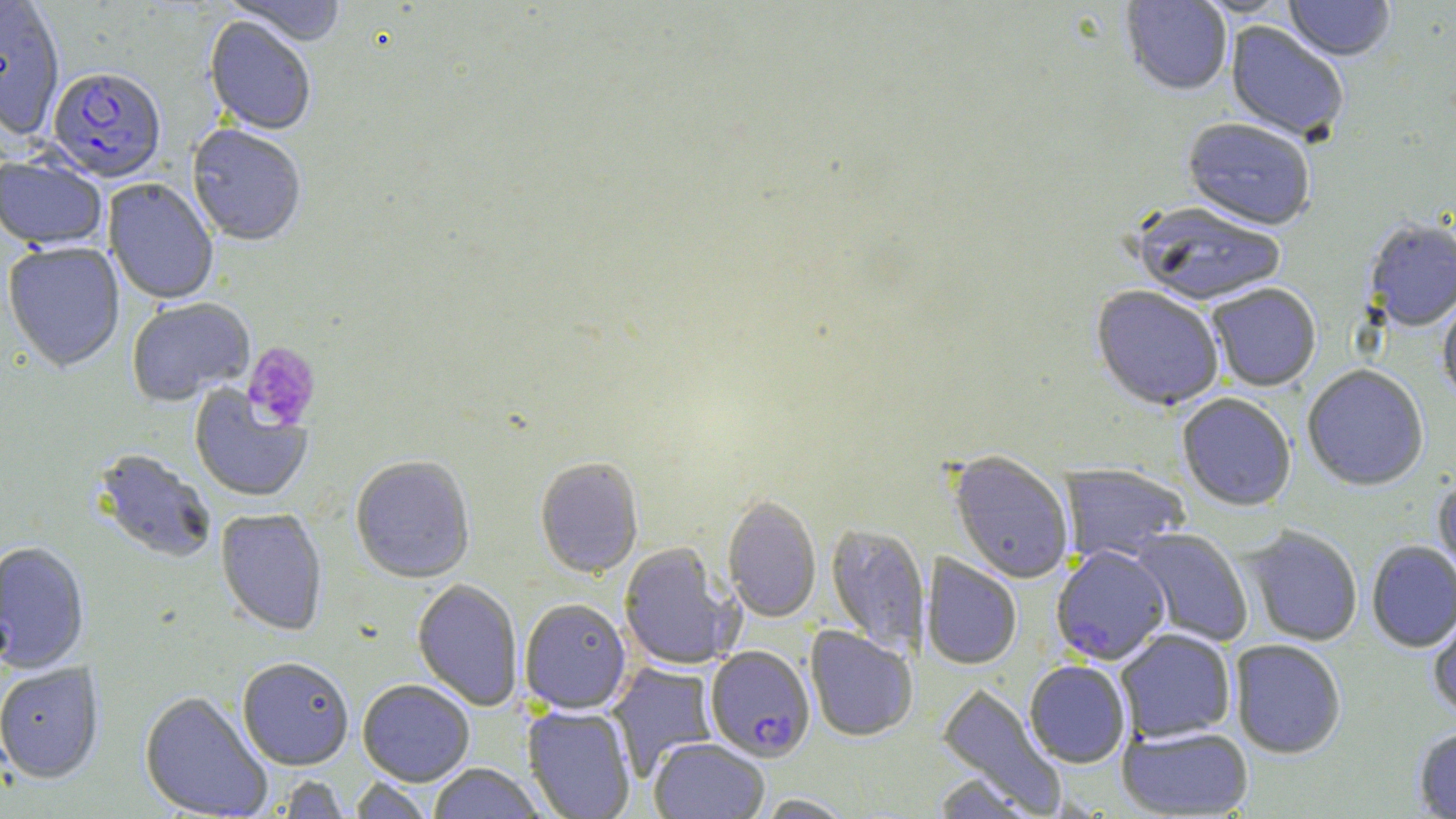
slide-level diagnosis = Plasmodium falciparum
platelet locations = approximate bounding boxes as [x1, y1, x2, y2] in pixels: [242, 341, 321, 431]
Plasmodium falciparum-infected red blood cell locations = approximate bounding boxes as [x1, y1, x2, y2] in pixels: [47, 69, 166, 186], [1051, 546, 1170, 664], [705, 646, 815, 762]
stain = May-Grünwald-Giemsa
preparation = thin blood film
modality = optical microscopy
uninfected red blood cell locations = approximate bounding boxes as [x1, y1, x2, y2] in pixels: [224, 0, 347, 48], [1121, 0, 1232, 96], [1191, 0, 1295, 18], [1284, 0, 1395, 63], [0, 2, 65, 142], [203, 17, 316, 137], [1225, 22, 1348, 144], [1182, 120, 1316, 232], [187, 127, 306, 248], [0, 156, 107, 253], [103, 179, 219, 305], [1130, 204, 1287, 309], [1364, 220, 1456, 332], [3, 243, 125, 374], [1207, 284, 1321, 392], [1090, 286, 1225, 412], [1438, 294, 1456, 406], [126, 298, 255, 407], [1302, 366, 1429, 492], [188, 385, 312, 503], [1176, 393, 1296, 512], [91, 448, 217, 565], [948, 450, 1074, 584], [350, 457, 475, 584], [534, 458, 644, 579], [1060, 463, 1191, 563], [1433, 476, 1456, 597], [722, 496, 821, 624], [215, 509, 328, 637], [826, 523, 929, 654], [1242, 526, 1363, 646], [1130, 527, 1253, 647], [0, 542, 89, 674], [1366, 542, 1456, 652], [618, 543, 743, 671], [921, 554, 1022, 669], [411, 579, 524, 712], [520, 599, 631, 714], [1427, 599, 1456, 721], [805, 626, 918, 741], [1115, 629, 1236, 743], [1230, 639, 1346, 759], [237, 658, 353, 771], [1024, 660, 1131, 768], [606, 662, 718, 779], [0, 663, 104, 784], [358, 680, 475, 786], [936, 682, 1067, 815], [139, 691, 272, 819], [523, 705, 636, 819], [1117, 725, 1253, 818], [1413, 726, 1456, 818], [649, 738, 769, 819], [428, 764, 545, 818], [932, 773, 1037, 818], [276, 775, 352, 818], [349, 777, 434, 819], [755, 794, 855, 818]
magnification = 1000x
field of view = single
image size = 1456×819 pixels